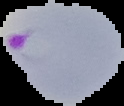

Summary:
  - Preparation: thin blood film
  - Image type: cell region segmented out of the field of view; surrounding area masked to black
  - Image size: 124×106 pixels
  - Result: malaria parasites detected